Classify this cell by malaria status.
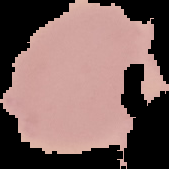

Uninfected.

image type = segmented cell region on a black background
image size = 169×169 pixels
preparation = thin blood film